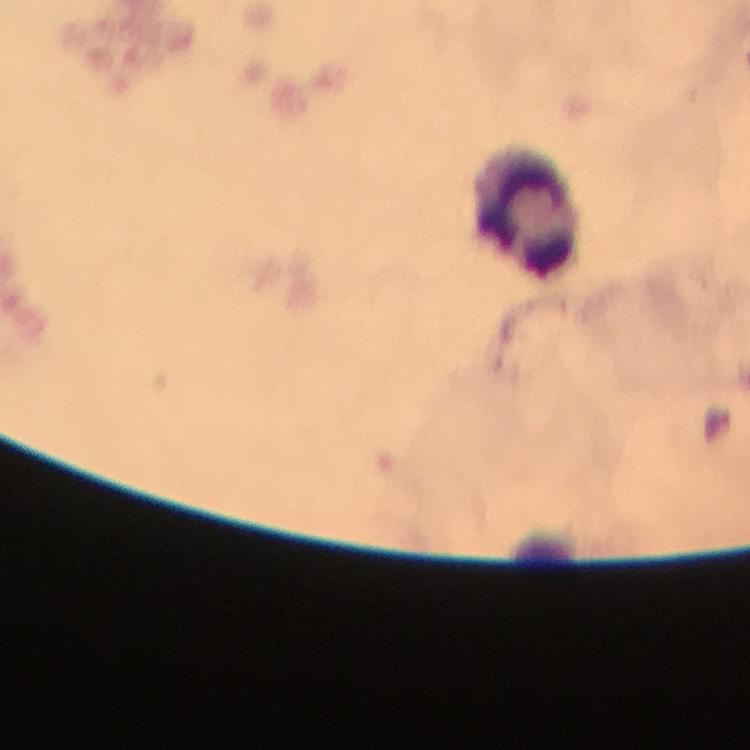

Approximate centers as (x, y) in pixels. Leukocyte locations: (522, 213). Immersion oil applied. Giemsa stain. At 100x magnification. Malaria parasites: none seen. Thick blood smear. A crop from one field of view. From a malaria diagnostic workup. Image is 750×750 pixels. Smartphone photograph taken through a microscope.